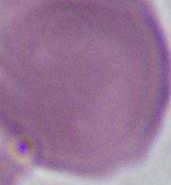
Photomicrograph. Captured at 1000x magnification. A red blood cell is shown.